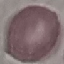
Malaria status: uninfected. Thin blood smear. Automatically extracted cell patch, resized to 64 × 64 pixels. Giemsa-stained preparation. Photographed with a smartphone camera at the microscope eyepiece.